Report the malaria status of this cell.
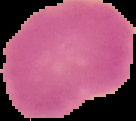

It is uninfected.

{
  "image_type": "cell region segmented out of the field of view; surrounding area masked to black",
  "image_size": "136×121 pixels",
  "preparation": "thin blood film"
}